Classify this cell by malaria status.
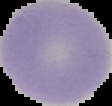

It is uninfected.

From a thin blood smear. Image is 112×106 pixels. Cell region segmented out of the field of view; the surrounding area is masked to black.